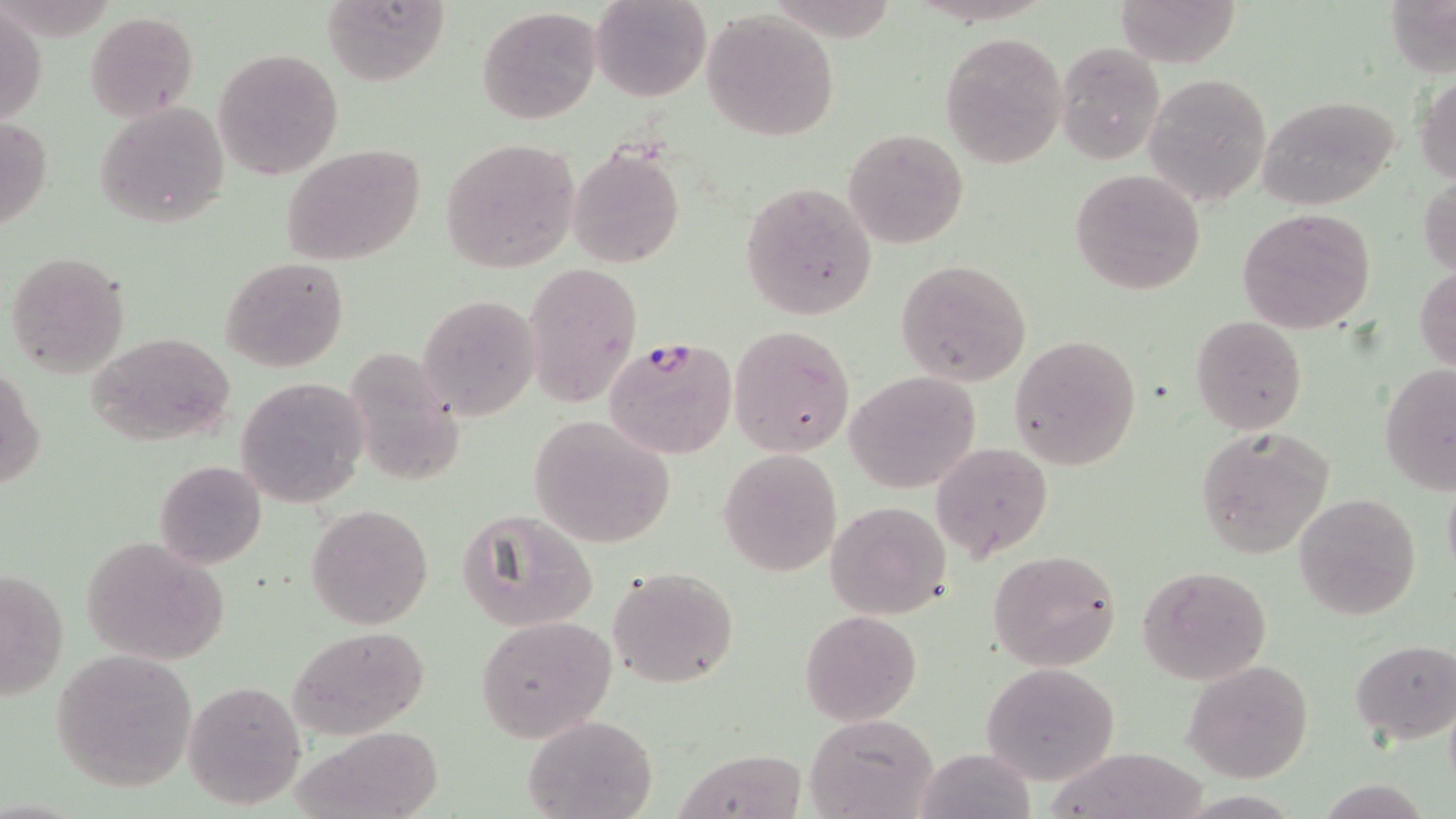
slide-level diagnosis = Plasmodium falciparum
stain = May-Grünwald-Giemsa
Plasmodium falciparum-infected red blood cell locations = approximate bounding boxes as (x1,y1)-(x2,y2) corner pairs in pixels: (603,335)-(738,461)
uninfected red blood cell locations = approximate bounding boxes as (x1,y1)-(x2,y2) corner pairs in pixels: (319,0)-(449,85), (591,0)-(711,102), (1112,0)-(1243,68), (1,4)-(45,129), (477,6)-(603,126), (701,8)-(841,141), (85,12)-(197,121), (941,33)-(1066,168), (1056,40)-(1166,164), (214,48)-(344,180), (1143,71)-(1272,209), (1415,75)-(1456,185), (1255,95)-(1401,209), (96,100)-(230,229), (1,111)-(51,239), (843,127)-(968,248), (441,138)-(581,273), (280,143)-(426,266), (569,145)-(684,267), (1069,168)-(1206,295), (1420,175)-(1456,276), (741,182)-(879,320), (1237,208)-(1376,334), (3,250)-(131,378), (218,256)-(350,372), (896,259)-(1032,387), (525,261)-(643,405), (1416,264)-(1455,375), (418,293)-(541,422), (1190,315)-(1308,437), (730,323)-(856,458), (87,332)-(237,448), (1009,334)-(1142,471), (1380,363)-(1456,495), (1,365)-(45,493), (843,370)-(983,493), (235,377)-(369,508), (528,415)-(676,548), (1194,425)-(1333,557), (930,440)-(1053,563), (718,447)-(841,577), (154,460)-(267,569), (1441,473)-(1456,588), (1293,492)-(1422,622), (826,501)-(951,619), (306,503)-(434,630), (458,510)-(598,633), (79,536)-(230,666), (987,550)-(1121,670), (0,562)-(69,708), (1140,565)-(1273,685), (608,566)-(739,689), (799,610)-(922,725), (474,616)-(618,742), (286,626)-(429,738), (1350,639)-(1456,746), (50,650)-(197,792), (1182,660)-(1314,783), (979,663)-(1120,786), (183,681)-(304,810), (804,713)-(939,819), (523,714)-(656,819), (676,747)-(807,819), (915,749)-(1034,818)
preparation = thin blood film
modality = optical microscopy
image size = 1456×819 pixels
magnification = 1000x
field of view = one of a larger specimen